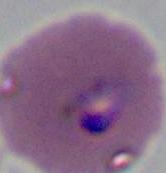

Photomicrograph. A Plasmodium parasite is shown. 400x or 1000x magnification.